Assess this cell for malaria.
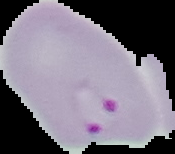
Parasitized.

image type = cell region segmented out of the field of view; surrounding area masked to black
image size = 175×154 pixels
preparation = thin blood smear